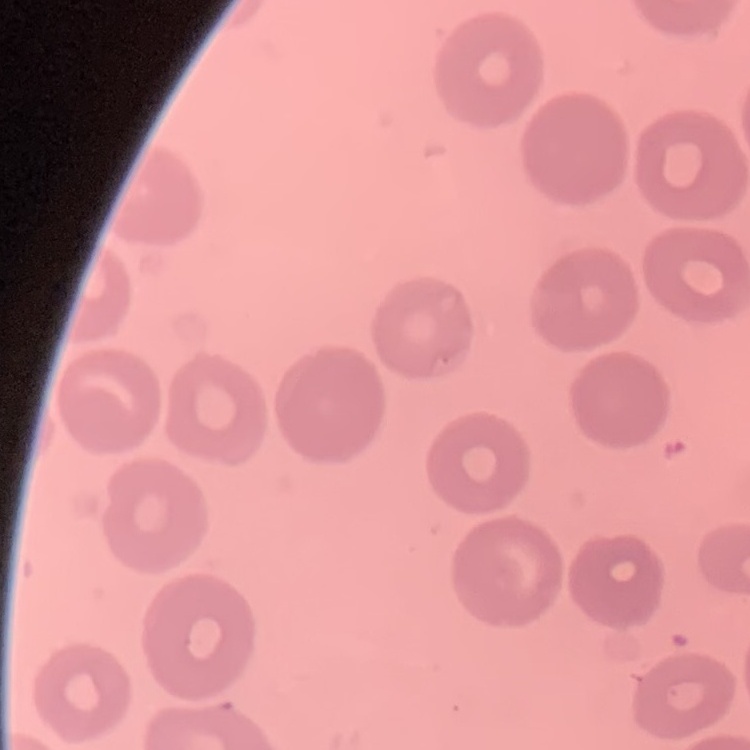 The red blood cells exhibit no rouleaux formation. Thin peripheral smear. Field's or Giemsa stain. Square crop of a larger photomicrograph.